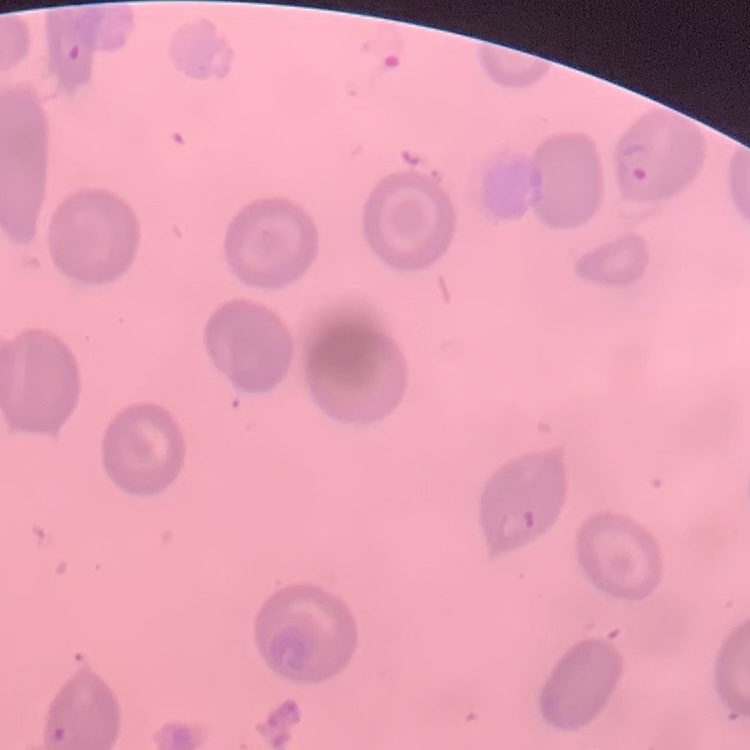 The red blood cells show no rouleaux formation. Stained with either Field's or Giemsa. Square crop of a larger photomicrograph. Thin peripheral smear.